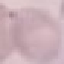
Summary:
  - Result: negative for malaria parasites
  - Capture: smartphone through the microscope eyepiece
  - Image type: automatically extracted cell patch, resized to 64 × 64 pixels
  - Preparation: thin blood smear
  - Stain: Giemsa